Evaluate for Plasmodium parasites.
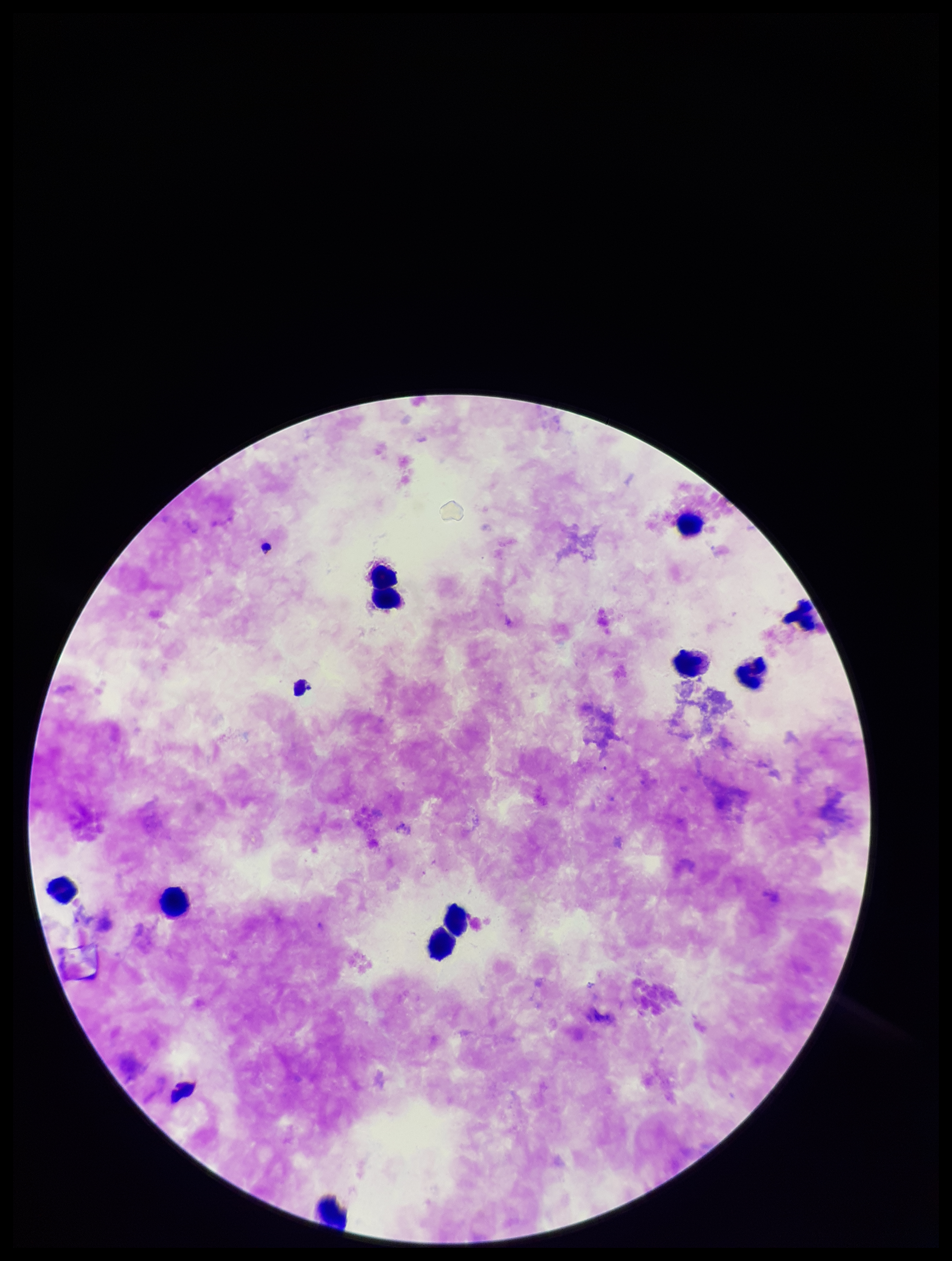

None detected.

image size = 952×1261 pixels
capture = smartphone photograph through the microscope eyepiece
parasite count = 0
stain = Giemsa
field of view = one from this slide
preparation = thick
leukocyte count = 10
patient malaria status = negative